Locate every blood parasite and identify its species.
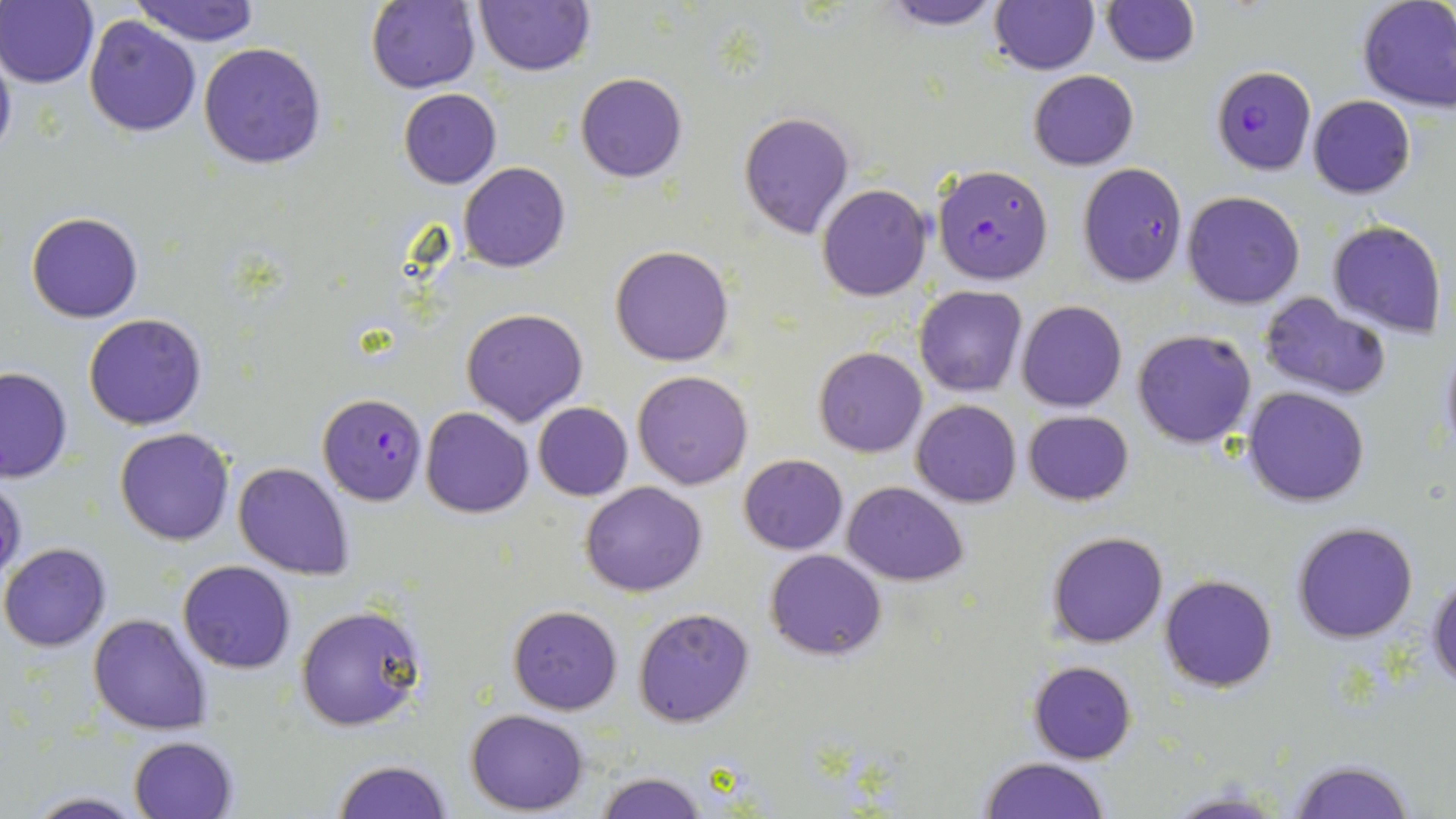
Approximate bounding boxes as (x1, y1, x2, y2) in pixels.
Plasmodium falciparum-infected red blood cells: (1211, 65, 1316, 175), (1077, 162, 1187, 287), (931, 163, 1053, 285), (318, 392, 428, 505).
No Plasmodium ovale, Plasmodium malariae, Plasmodium vivax, Babesia divergens, or Trypanosoma brucei observed.

Uninfected red blood cell locations: (1, 0, 98, 87), (473, 0, 595, 76), (876, 0, 1009, 29), (989, 0, 1100, 75), (1099, 0, 1200, 67), (1357, 0, 1456, 115), (131, 1, 260, 46), (367, 1, 480, 93), (83, 15, 201, 137), (0, 36, 17, 167), (197, 43, 327, 169), (1028, 70, 1139, 171), (576, 71, 688, 182), (398, 88, 501, 189), (1307, 95, 1416, 198), (738, 111, 855, 239), (458, 162, 571, 273), (817, 183, 932, 301), (1181, 191, 1305, 309), (27, 212, 143, 323), (1328, 220, 1448, 338), (610, 243, 736, 366), (915, 286, 1026, 397), (1260, 293, 1391, 400), (1016, 300, 1127, 413), (462, 309, 586, 426), (82, 312, 207, 431), (1132, 328, 1257, 448), (1436, 337, 1456, 462), (813, 348, 927, 458), (0, 367, 73, 483), (632, 370, 753, 489), (1242, 386, 1370, 508), (911, 399, 1022, 507), (534, 402, 633, 501), (421, 406, 533, 517), (1022, 410, 1135, 506), (116, 427, 235, 546), (739, 454, 848, 554), (232, 460, 355, 580), (1, 476, 27, 585), (580, 481, 708, 597), (842, 482, 969, 584), (1291, 521, 1418, 642), (1045, 531, 1168, 648), (0, 543, 111, 651), (765, 549, 887, 661), (178, 560, 298, 674), (1160, 573, 1279, 692), (1429, 574, 1456, 693), (296, 603, 429, 733), (507, 605, 624, 714), (633, 607, 755, 727), (89, 613, 215, 735), (1028, 660, 1137, 765), (465, 709, 587, 814), (130, 735, 239, 819), (977, 756, 1113, 818), (333, 759, 455, 819), (1286, 759, 1415, 819), (597, 770, 707, 819), (1160, 786, 1295, 818), (18, 791, 152, 819). Slide-level diagnosis: Plasmodium falciparum. Image is 1456×819 pixels. One field of a larger specimen. Light microscopy. Thin blood film. May-Grünwald-Giemsa stain. 1000x magnification.